Outline each blood parasite and name the species.
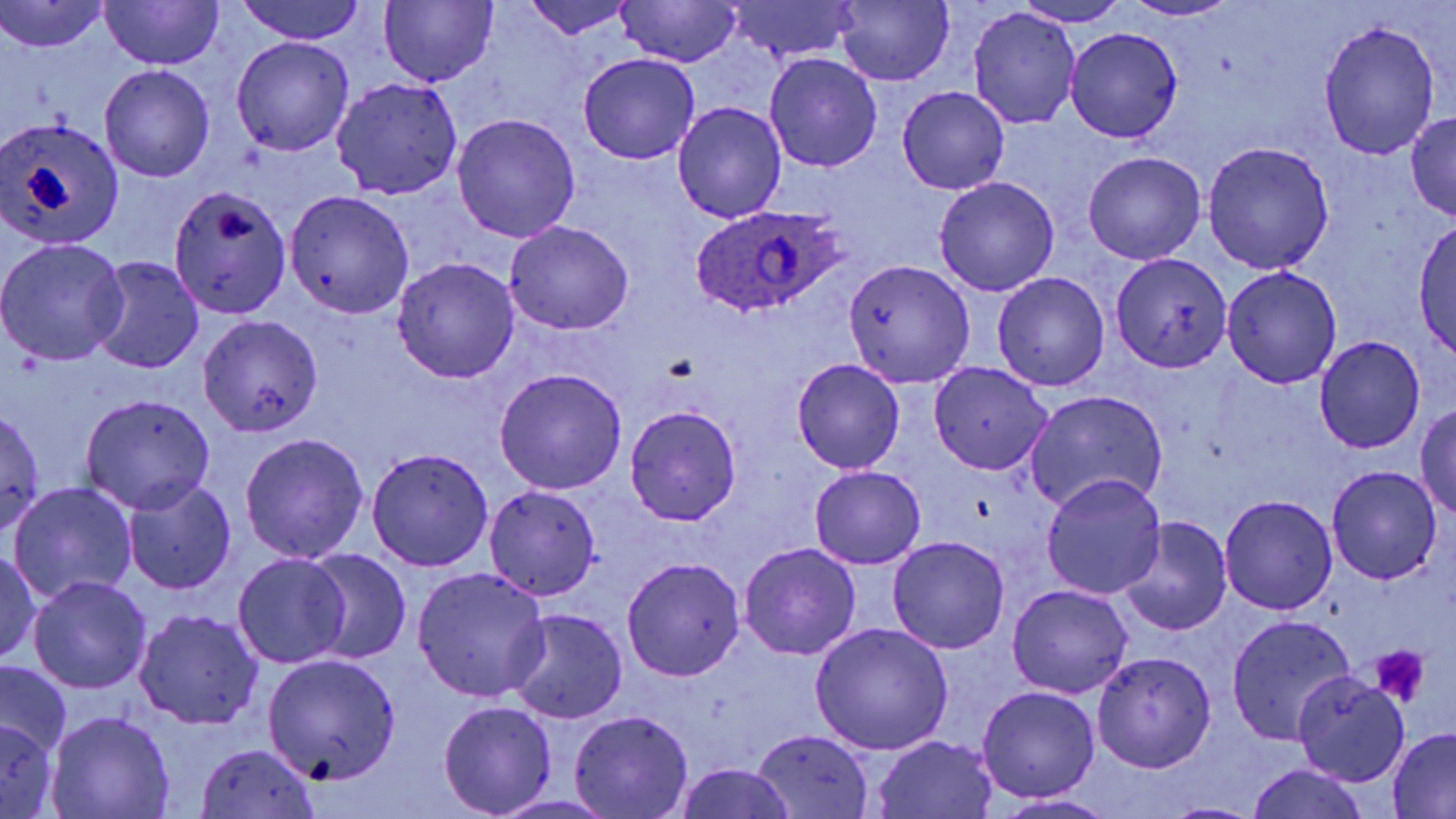
Approximate bounding boxes as [x1, y1, x2, y2] in pixels.
Plasmodium ovale-infected red blood cells: [688, 204, 849, 321].
No Plasmodium falciparum, Plasmodium malariae, Plasmodium vivax, Babesia divergens, or Trypanosoma brucei observed.

Uninfected red blood cell locations: [100, 0, 222, 70], [235, 0, 364, 45], [379, 0, 497, 87], [517, 0, 640, 41], [724, 0, 861, 60], [0, 1, 111, 55], [1016, 1, 1128, 26], [1124, 1, 1241, 21], [615, 2, 743, 67], [832, 2, 954, 86], [968, 9, 1080, 127], [1317, 21, 1440, 159], [1065, 27, 1183, 142], [231, 36, 354, 155], [764, 52, 883, 173], [579, 54, 701, 164], [100, 65, 214, 181], [332, 77, 462, 199], [898, 87, 1009, 195], [673, 102, 787, 221], [1406, 112, 1456, 218], [452, 113, 581, 243], [0, 116, 125, 249], [1202, 141, 1335, 273], [1082, 150, 1207, 265], [935, 176, 1059, 295], [167, 184, 289, 317], [286, 191, 414, 317], [504, 219, 635, 335], [1413, 220, 1456, 362], [0, 237, 130, 366], [1109, 252, 1231, 373], [90, 255, 204, 374], [391, 258, 520, 383], [843, 259, 973, 386], [1221, 266, 1342, 390], [992, 272, 1110, 392], [200, 315, 324, 435], [1315, 336, 1425, 453], [791, 358, 906, 472], [928, 362, 1053, 474], [493, 367, 628, 494], [1026, 390, 1169, 516], [82, 394, 215, 514], [1414, 403, 1456, 518], [624, 405, 743, 526], [0, 407, 46, 538], [238, 433, 369, 563], [367, 448, 494, 571], [809, 466, 926, 569], [1325, 466, 1443, 584], [1041, 474, 1167, 598], [122, 475, 236, 596], [9, 481, 137, 606], [484, 485, 601, 600], [1218, 494, 1337, 615], [1119, 518, 1232, 637], [888, 537, 1010, 652], [738, 542, 861, 661], [0, 546, 42, 663], [303, 548, 412, 665], [234, 554, 351, 670], [622, 557, 745, 681], [411, 567, 552, 704], [29, 576, 151, 692], [1007, 584, 1134, 699], [133, 608, 263, 730], [505, 608, 628, 724], [1225, 614, 1357, 744], [810, 623, 954, 755], [1090, 650, 1217, 773], [262, 653, 402, 785], [0, 663, 72, 756], [1292, 673, 1411, 787], [977, 686, 1099, 801], [439, 700, 556, 816], [47, 709, 175, 818], [569, 709, 694, 819], [0, 722, 60, 815], [1387, 729, 1456, 818], [752, 730, 874, 817], [873, 735, 998, 817], [194, 743, 323, 818], [1246, 762, 1371, 819], [675, 763, 797, 819], [989, 794, 1119, 818], [491, 796, 622, 818], [1156, 800, 1268, 818]. Platelet locations: [664, 353, 697, 382], [1371, 644, 1431, 706]. Slide-level diagnosis: Plasmodium ovale. One field of a larger specimen. Image is 1456×819 pixels. Thin blood smear. May-Grünwald-Giemsa stain. 1000x magnification. Optical microscopy.